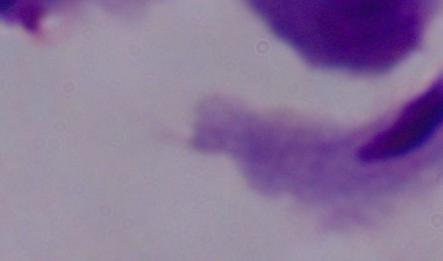
identification = trichomonad
magnification = 1000x
modality = photomicrograph